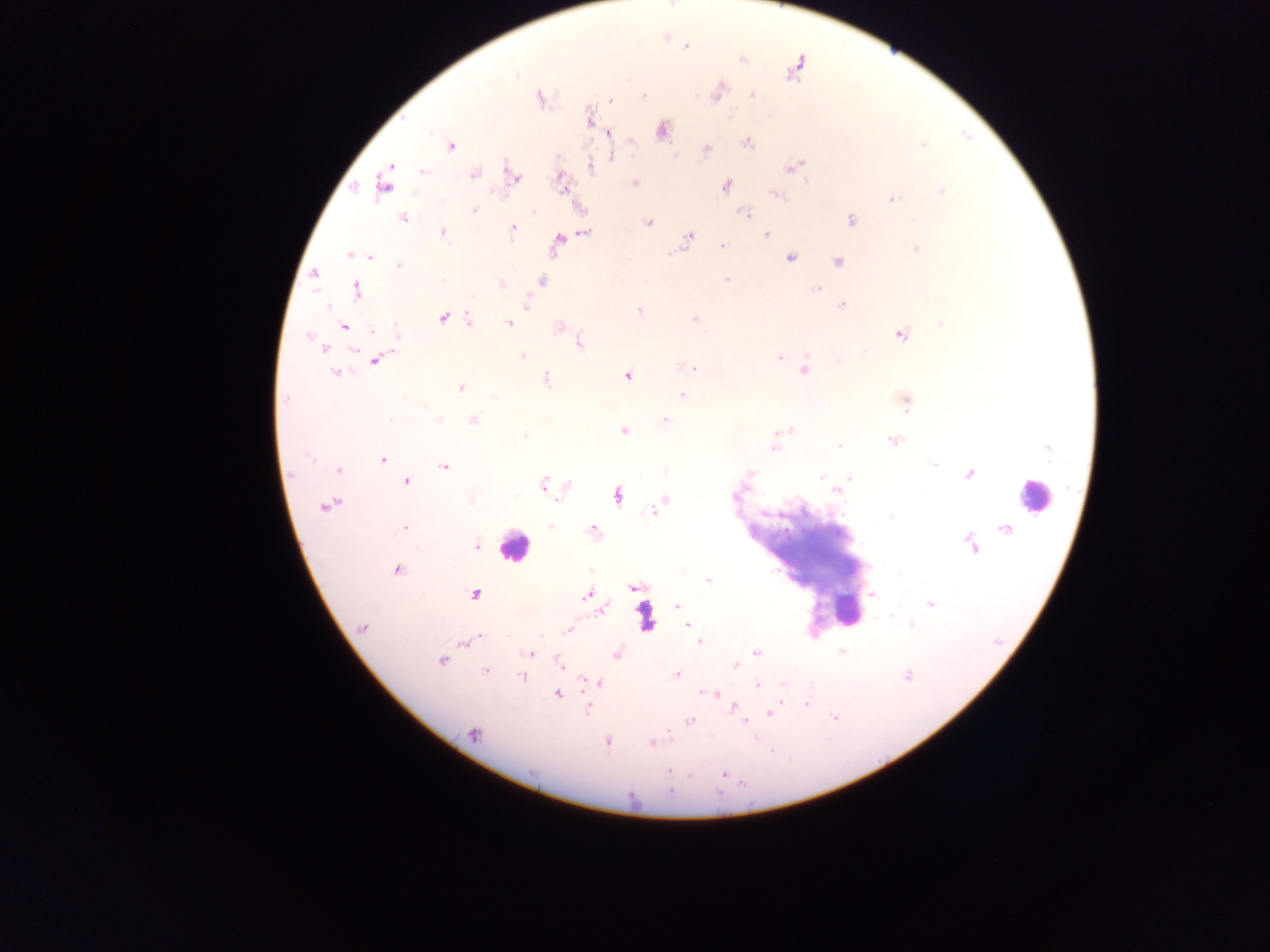 Approximate centers as (x, y) in pixels. Leukocyte locations: (1033, 496), (513, 545), (847, 612). Plasmodium parasite locations: (686, 47), (742, 59), (793, 70), (516, 74), (475, 88), (718, 93), (643, 95), (753, 95), (540, 98), (610, 101), (589, 119), (661, 131), (608, 133), (747, 143), (924, 145), (451, 146), (706, 150), (613, 156), (390, 165), (590, 166), (793, 167), (388, 172), (423, 172), (473, 174), (513, 177), (561, 178), (635, 183), (384, 184), (727, 185), (562, 188), (941, 191), (415, 193), (775, 195), (891, 199), (442, 201), (474, 210), (746, 214), (403, 218), (851, 220), (648, 223), (512, 228), (585, 232), (443, 233), (766, 235), (688, 238), (557, 243), (722, 246), (916, 248), (349, 254), (370, 256), (791, 257), (838, 261), (399, 265), (314, 274), (727, 279), (442, 280), (542, 281), (502, 285), (816, 288), (357, 291), (527, 302), (842, 304), (328, 306), (638, 310), (442, 318), (469, 318), (695, 319), (508, 323), (940, 324), (344, 326), (558, 327), (372, 331), (397, 331), (901, 335), (309, 336), (580, 343), (323, 349), (864, 353), (522, 356), (779, 358), (376, 360), (683, 367), (694, 369), (805, 370), (335, 373), (628, 376), (546, 379), (461, 388), (682, 395), (494, 398), (286, 399), (905, 403), (425, 406), (390, 418), (440, 419), (474, 420), (665, 420), (788, 429), (623, 431), (782, 431), (524, 436), (894, 440), (839, 446), (774, 447), (1049, 450), (309, 457), (382, 459), (932, 464), (444, 466), (338, 469), (749, 473), (969, 474), (821, 477), (850, 478), (407, 482), (544, 484), (568, 484), (837, 491), (618, 495), (734, 495), (664, 499), (471, 500), (325, 505), (658, 506), (652, 511), (890, 517), (550, 526), (404, 529), (593, 530), (971, 544), (477, 546), (397, 570), (709, 581), (634, 588), (474, 594), (586, 595), (873, 595), (930, 603), (677, 606), (603, 610), (911, 624), (688, 626), (362, 627), (568, 629), (540, 635), (478, 638), (699, 642), (464, 643), (757, 652), (842, 652), (529, 655), (617, 655), (440, 661), (559, 664), (736, 666), (485, 672), (676, 674), (907, 676), (521, 678), (601, 683), (784, 683), (758, 685), (706, 693), (714, 694), (558, 695), (807, 704), (733, 707), (588, 708), (770, 713), (835, 717), (689, 721), (744, 722), (474, 735), (607, 743), (652, 744), (668, 770), (724, 774), (670, 791). Thick blood film. Image is 1270×952 pixels. Single field of view. Photographed through a microscope with a mobile-phone camera. Sample from Ghana.